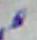

Micrograph. Toxoplasma gondii is seen. Captured at 1000x magnification.